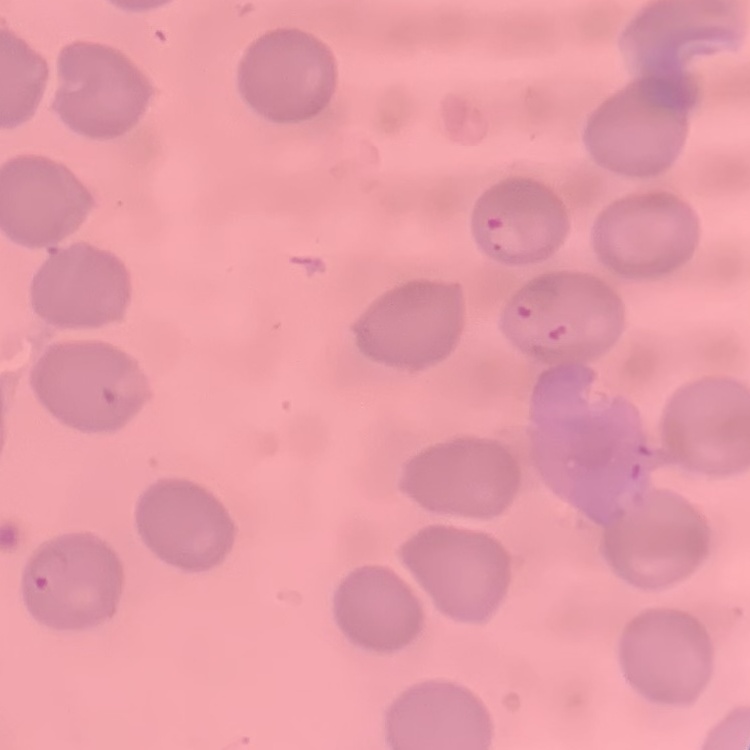 The red blood cells exhibit no rouleaux formation. One tile cut from a larger photomicrograph. Thin peripheral smear. Stained with either Field's or Giemsa.